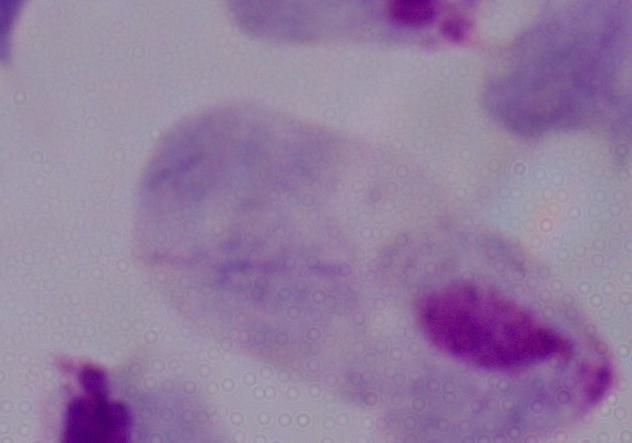

Summary:
  - Magnification: 1000x
  - Modality: photomicrograph
  - Identification: trichomonad